Identify the cell.
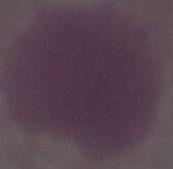

An erythrocyte.

Photomicrograph. 1000x magnification.